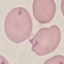

Summary:
  - Result: negative for malaria parasites
  - Capture: smartphone through the microscope eyepiece
  - Preparation: thin blood film
  - Image type: automatically extracted cell patch, resized to 64 × 64 pixels
  - Stain: Giemsa